Describe the morphology of the red blood cells.
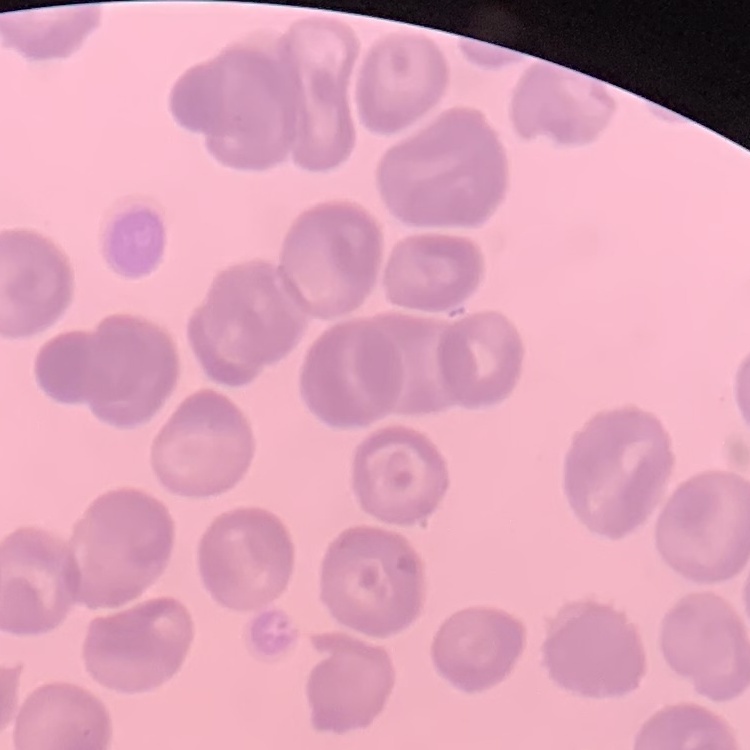

No rouleaux formation.

Thin peripheral smear. One tile cut from a larger photomicrograph. Stained with either Field's or Giemsa.